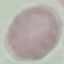 Malaria status: uninfected. Automatically extracted cell patch, resized to 64 × 64 pixels. Acquired by smartphone through the microscope eyepiece. Thin smear of blood. Giemsa-stained preparation.